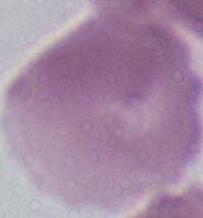 Micrograph. 1000x magnification. A red blood cell is seen.